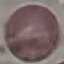

malaria status = uninfected
preparation = thin blood film
image type = cell patch, automatically extracted from a larger field of view and resized to 64 × 64 pixels
capture = smartphone camera at the microscope eyepiece
stain = Giemsa